Report the malaria status of this cell.
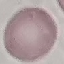

Uninfected.

Giemsa stain. Cell patch, automatically extracted from a larger field of view and resized to 64 × 64 pixels. Photographed with a smartphone camera at the microscope eyepiece. Thin smear of blood.